Assess this cell for malaria.
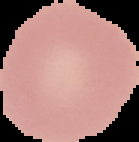
It is uninfected.

Summary:
  - Image type: segmented cell region on a black background
  - Preparation: thin blood film
  - Image size: 139×142 pixels